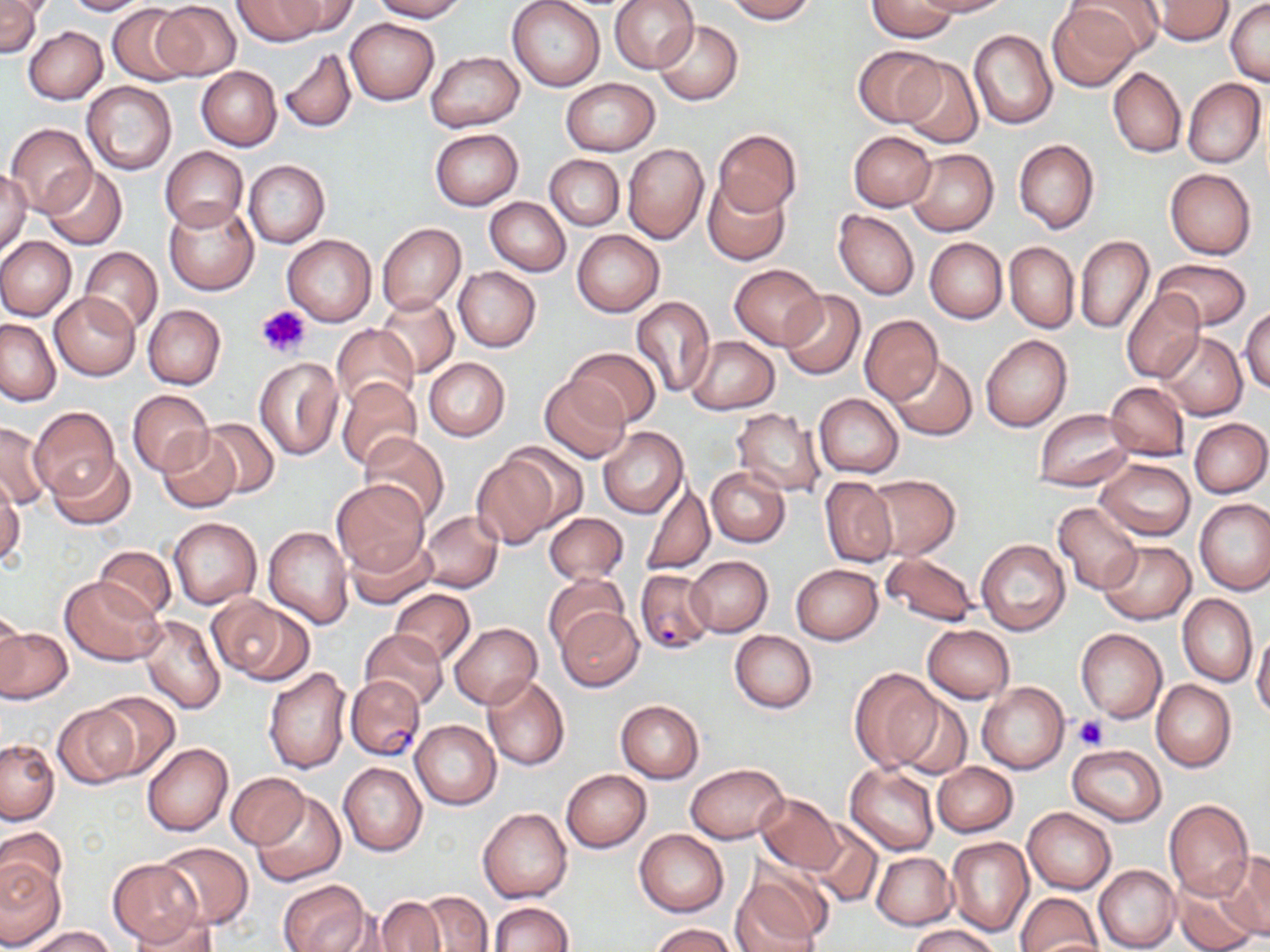

Approximate bounding boxes as named x1/y1/x2/y2 corners in pixels. Uninfected red blood cell locations: (x1=0, y1=0, x2=42, y2=57), (x1=62, y1=0, x2=151, y2=15), (x1=232, y1=0, x2=326, y2=46), (x1=274, y1=0, x2=359, y2=36), (x1=370, y1=0, x2=467, y2=21), (x1=507, y1=0, x2=605, y2=91), (x1=610, y1=0, x2=698, y2=73), (x1=719, y1=0, x2=817, y2=23), (x1=912, y1=0, x2=1012, y2=17), (x1=1070, y1=0, x2=1165, y2=58), (x1=1148, y1=0, x2=1234, y2=44), (x1=151, y1=1, x2=241, y2=80), (x1=866, y1=1, x2=956, y2=42), (x1=1226, y1=3, x2=1270, y2=84), (x1=107, y1=4, x2=191, y2=85), (x1=1051, y1=4, x2=1148, y2=87), (x1=345, y1=19, x2=439, y2=104), (x1=655, y1=20, x2=743, y2=105), (x1=24, y1=26, x2=107, y2=103), (x1=969, y1=29, x2=1057, y2=129), (x1=853, y1=45, x2=946, y2=127), (x1=279, y1=48, x2=357, y2=135), (x1=425, y1=52, x2=523, y2=133), (x1=896, y1=58, x2=982, y2=148), (x1=196, y1=66, x2=281, y2=150), (x1=1108, y1=66, x2=1186, y2=158), (x1=560, y1=78, x2=659, y2=156), (x1=1183, y1=79, x2=1265, y2=167), (x1=82, y1=81, x2=177, y2=175), (x1=5, y1=123, x2=97, y2=215), (x1=430, y1=128, x2=523, y2=210), (x1=715, y1=129, x2=800, y2=216), (x1=849, y1=130, x2=935, y2=211), (x1=1013, y1=139, x2=1099, y2=234), (x1=623, y1=142, x2=709, y2=244), (x1=161, y1=146, x2=247, y2=231), (x1=905, y1=149, x2=998, y2=236), (x1=545, y1=154, x2=623, y2=230), (x1=244, y1=160, x2=330, y2=247), (x1=40, y1=165, x2=127, y2=250), (x1=0, y1=167, x2=32, y2=258), (x1=1164, y1=168, x2=1257, y2=259), (x1=704, y1=177, x2=789, y2=264), (x1=485, y1=197, x2=571, y2=276), (x1=164, y1=199, x2=257, y2=295), (x1=834, y1=210, x2=919, y2=299), (x1=376, y1=223, x2=466, y2=315), (x1=572, y1=230, x2=664, y2=316), (x1=282, y1=235, x2=376, y2=326), (x1=1075, y1=235, x2=1153, y2=334), (x1=0, y1=237, x2=75, y2=320), (x1=924, y1=238, x2=1006, y2=324), (x1=1005, y1=241, x2=1078, y2=332), (x1=79, y1=246, x2=163, y2=335), (x1=1153, y1=259, x2=1251, y2=331), (x1=730, y1=264, x2=826, y2=349), (x1=453, y1=266, x2=542, y2=351), (x1=1120, y1=289, x2=1204, y2=383), (x1=778, y1=290, x2=865, y2=379), (x1=51, y1=293, x2=140, y2=379), (x1=379, y1=297, x2=458, y2=376), (x1=631, y1=297, x2=715, y2=398), (x1=143, y1=304, x2=226, y2=389), (x1=1240, y1=305, x2=1269, y2=393), (x1=859, y1=314, x2=942, y2=405), (x1=1, y1=318, x2=61, y2=406), (x1=331, y1=324, x2=419, y2=409), (x1=1157, y1=332, x2=1248, y2=421), (x1=980, y1=335, x2=1072, y2=432), (x1=686, y1=337, x2=780, y2=414), (x1=565, y1=348, x2=662, y2=427), (x1=886, y1=355, x2=976, y2=440), (x1=254, y1=357, x2=343, y2=459), (x1=423, y1=358, x2=509, y2=442), (x1=540, y1=375, x2=632, y2=463), (x1=336, y1=376, x2=423, y2=471), (x1=1104, y1=381, x2=1190, y2=461), (x1=128, y1=389, x2=213, y2=476), (x1=814, y1=394, x2=904, y2=477), (x1=30, y1=406, x2=119, y2=500), (x1=732, y1=408, x2=827, y2=499), (x1=1034, y1=408, x2=1134, y2=490), (x1=197, y1=417, x2=281, y2=499), (x1=1188, y1=417, x2=1269, y2=498), (x1=1, y1=421, x2=50, y2=508), (x1=597, y1=427, x2=688, y2=519), (x1=156, y1=431, x2=242, y2=514), (x1=359, y1=432, x2=450, y2=525), (x1=496, y1=441, x2=587, y2=531), (x1=471, y1=451, x2=561, y2=547), (x1=48, y1=454, x2=136, y2=529), (x1=1096, y1=459, x2=1195, y2=540), (x1=707, y1=467, x2=790, y2=546), (x1=821, y1=475, x2=898, y2=568), (x1=865, y1=475, x2=961, y2=560), (x1=0, y1=476, x2=22, y2=567), (x1=332, y1=480, x2=430, y2=575), (x1=640, y1=481, x2=716, y2=576), (x1=1194, y1=498, x2=1270, y2=595), (x1=1053, y1=501, x2=1143, y2=595), (x1=420, y1=511, x2=502, y2=593), (x1=544, y1=513, x2=628, y2=585), (x1=167, y1=517, x2=263, y2=609), (x1=264, y1=526, x2=352, y2=628), (x1=345, y1=537, x2=436, y2=609), (x1=975, y1=538, x2=1069, y2=636), (x1=1099, y1=541, x2=1195, y2=624), (x1=94, y1=545, x2=176, y2=621), (x1=880, y1=552, x2=980, y2=627), (x1=687, y1=556, x2=773, y2=637), (x1=791, y1=564, x2=883, y2=645), (x1=544, y1=574, x2=628, y2=652), (x1=60, y1=575, x2=165, y2=665), (x1=389, y1=588, x2=475, y2=665), (x1=1178, y1=594, x2=1257, y2=687), (x1=212, y1=597, x2=313, y2=684), (x1=96, y1=601, x2=202, y2=708), (x1=0, y1=604, x2=28, y2=692), (x1=556, y1=606, x2=644, y2=690), (x1=139, y1=614, x2=226, y2=713), (x1=449, y1=622, x2=542, y2=708), (x1=923, y1=624, x2=1015, y2=704), (x1=1, y1=626, x2=72, y2=703), (x1=1074, y1=628, x2=1167, y2=723), (x1=359, y1=629, x2=449, y2=710), (x1=730, y1=630, x2=816, y2=713), (x1=1251, y1=630, x2=1270, y2=720), (x1=263, y1=667, x2=352, y2=775), (x1=849, y1=668, x2=943, y2=772), (x1=482, y1=675, x2=570, y2=771), (x1=1152, y1=679, x2=1236, y2=772), (x1=977, y1=682, x2=1070, y2=773), (x1=92, y1=691, x2=181, y2=780), (x1=893, y1=692, x2=972, y2=780), (x1=615, y1=699, x2=704, y2=782), (x1=54, y1=705, x2=138, y2=788), (x1=410, y1=720, x2=501, y2=810), (x1=0, y1=740, x2=59, y2=824), (x1=142, y1=743, x2=233, y2=836), (x1=1067, y1=745, x2=1166, y2=825), (x1=931, y1=761, x2=1018, y2=837), (x1=338, y1=762, x2=427, y2=856), (x1=685, y1=762, x2=788, y2=843), (x1=845, y1=764, x2=939, y2=856), (x1=561, y1=769, x2=651, y2=852), (x1=227, y1=772, x2=307, y2=848), (x1=250, y1=789, x2=346, y2=886), (x1=756, y1=792, x2=843, y2=876), (x1=1165, y1=800, x2=1253, y2=901), (x1=1023, y1=807, x2=1116, y2=893), (x1=477, y1=808, x2=573, y2=903), (x1=806, y1=820, x2=883, y2=909), (x1=0, y1=827, x2=67, y2=902), (x1=635, y1=829, x2=728, y2=916), (x1=946, y1=837, x2=1034, y2=936), (x1=156, y1=843, x2=253, y2=929), (x1=872, y1=853, x2=957, y2=929), (x1=1222, y1=853, x2=1270, y2=939), (x1=0, y1=859, x2=66, y2=947), (x1=107, y1=859, x2=203, y2=945), (x1=1094, y1=865, x2=1180, y2=952), (x1=732, y1=867, x2=829, y2=950), (x1=277, y1=878, x2=369, y2=952), (x1=1173, y1=879, x2=1260, y2=952), (x1=415, y1=890, x2=492, y2=951), (x1=1015, y1=892, x2=1102, y2=952), (x1=371, y1=897, x2=444, y2=951), (x1=487, y1=902, x2=574, y2=952), (x1=127, y1=908, x2=218, y2=952), (x1=15, y1=910, x2=99, y2=949), (x1=650, y1=922, x2=739, y2=952), (x1=908, y1=923, x2=1000, y2=952), (x1=23, y1=926, x2=118, y2=951). Platelet locations: (x1=256, y1=304, x2=311, y2=358), (x1=1073, y1=714, x2=1109, y2=750). Plasmodium falciparum-infected red blood cell locations: (x1=635, y1=569, x2=715, y2=655), (x1=348, y1=676, x2=425, y2=759). Slide-level diagnosis: Plasmodium falciparum. Captured at 1000x magnification. May-Grünwald-Giemsa stain. Image is 1270×952 pixels. One field of a larger specimen. Thin blood smear. Light microscopy.